Assess this cell for malaria.
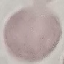

It is uninfected.

Giemsa stain. Thin blood film. Photographed with a smartphone camera at the microscope eyepiece. Automatically extracted cell patch, resized to 64 × 64 pixels.